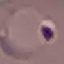
Malaria status: parasitized. Photographed with a smartphone camera at the microscope eyepiece. Automatically extracted cell patch, resized to 64 × 64 pixels. Giemsa-stained preparation. Thin blood film.